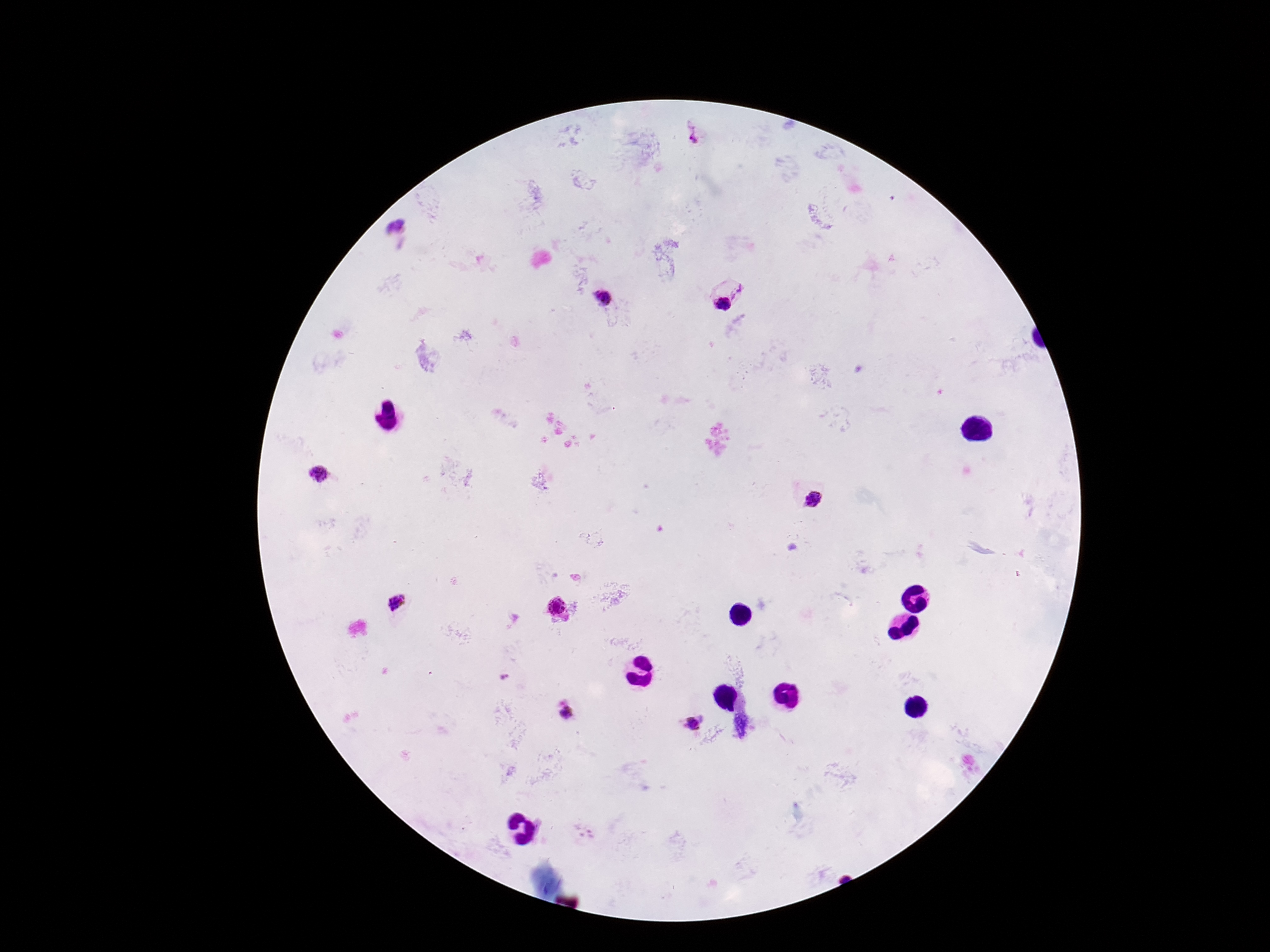
stain: Giemsa
magnification: 100x
image_size: 1270×952 pixels
patient_malaria_status: infected
field_of_view: one from this slide
plasmodium_parasite_locations: 'approximate centers as {x, y} in pixels: {695, 136}, {395, 227}, {740, 293}, {604, 298}, {724, 303}, {318, 474}, {814, 500}, {396, 604}, {556, 608}, {565, 714}, {694, 724}'
preparation: thick blood film
capture: smartphone camera through the microscope eyepiece